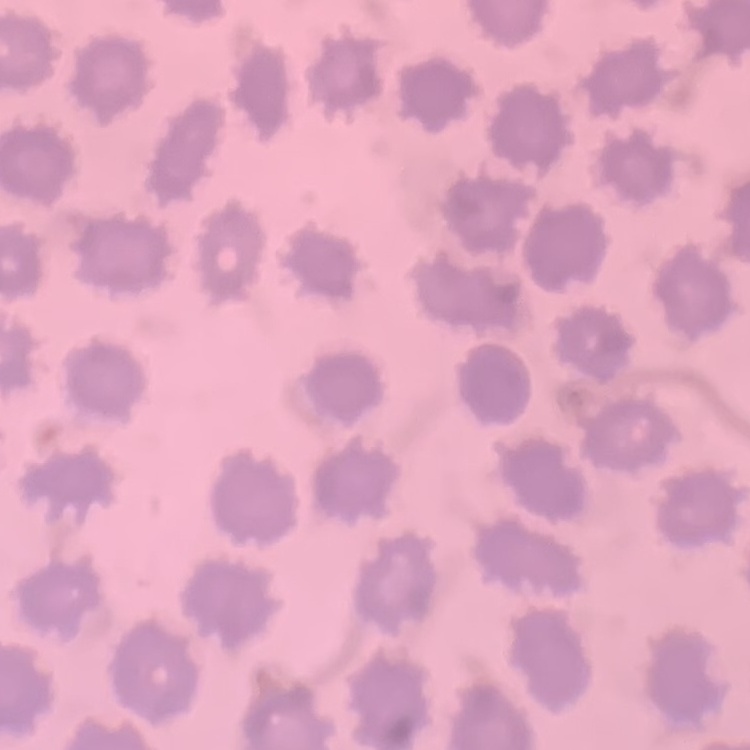

The red blood cells exhibit no rouleaux formation. Thin blood film. One tile cut from a larger photomicrograph. Stained with either Field's or Giemsa.